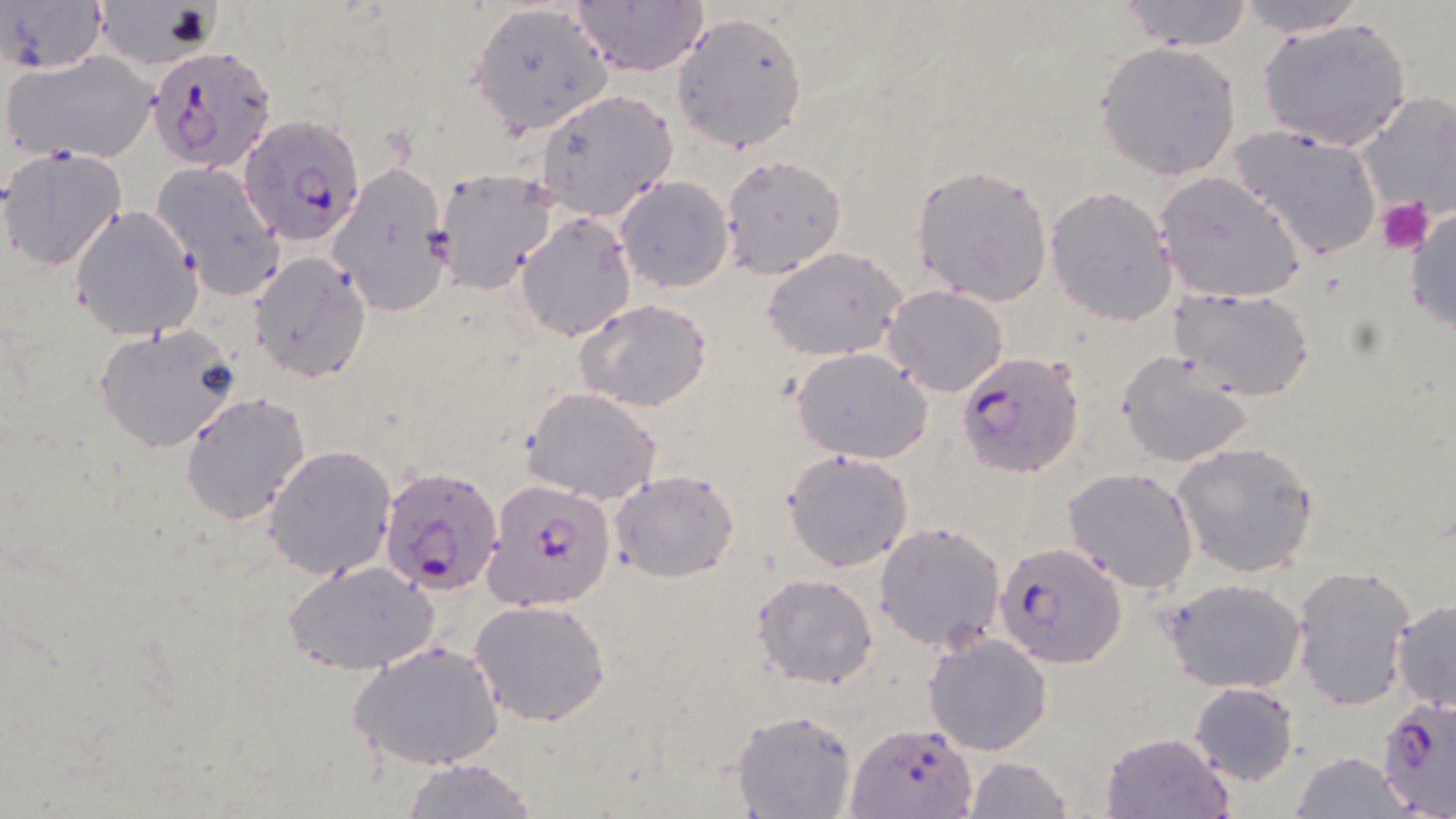

Summary:
  - Coordinate format: approximate bounding boxes as [x1, y1, x2, y2] in pixels
  - Uninfected red blood cell locations (subset): [0, 0, 110, 78], [1116, 0, 1256, 50], [91, 1, 223, 69], [571, 1, 710, 77], [1236, 1, 1367, 36], [470, 2, 613, 135], [671, 12, 810, 153], [1258, 16, 1413, 154], [1094, 40, 1243, 181], [2, 50, 159, 164], [535, 89, 678, 222], [1350, 90, 1456, 227], [1227, 125, 1384, 261], [0, 145, 127, 270], [719, 154, 848, 280], [326, 161, 453, 317], [149, 163, 285, 297], [911, 163, 1056, 307], [435, 169, 560, 293], [1154, 171, 1306, 304], [615, 175, 736, 294], [1046, 186, 1179, 325], [1406, 204, 1456, 340], [70, 205, 203, 342], [514, 212, 637, 342], [761, 246, 909, 361], [249, 253, 372, 383], [883, 285, 1009, 397], [1171, 285, 1316, 402], [576, 299, 712, 412], [93, 323, 244, 453], [792, 348, 932, 462], [1115, 350, 1256, 468], [522, 387, 662, 504], [179, 392, 312, 524], [1171, 442, 1320, 577], [263, 444, 397, 580], [783, 450, 912, 572], [1062, 468, 1198, 593], [610, 469, 740, 583], [873, 520, 1005, 652], [284, 561, 439, 677], [1290, 563, 1417, 711], [752, 573, 879, 690], [1163, 576, 1308, 693], [1389, 598, 1456, 716], [468, 599, 611, 726], [922, 632, 1054, 756], [348, 640, 505, 773], [1188, 681, 1300, 786], [731, 710, 856, 818], [1100, 730, 1234, 819], [1289, 752, 1414, 819], [961, 756, 1074, 819], [398, 758, 541, 817]
  - Plasmodium falciparum-infected red blood cell locations (subset): [147, 43, 273, 169], [238, 114, 366, 245], [956, 350, 1085, 479], [379, 464, 505, 597], [484, 478, 617, 611], [1376, 700, 1456, 819], [846, 721, 976, 818]
  - Platelet locations: [1378, 198, 1433, 254]
  - Slide-level diagnosis: Plasmodium falciparum
  - Stain: May-Grünwald-Giemsa
  - Preparation: thin blood smear
  - Magnification: 1000x
  - Image size: 1456×819 pixels
  - Modality: optical microscopy
  - Field of view: single